Assess this cell for malaria.
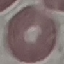

Uninfected.

Photographed with a smartphone camera at the microscope eyepiece. Giemsa-stained preparation. Thin blood film. Cell patch, automatically extracted from a larger field of view and resized to 64 × 64 pixels.